Identify the parasite.
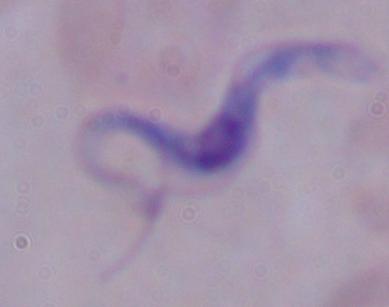
This is a trypanosome.

magnification = 1000x
modality = micrograph